Assess this cell for malaria.
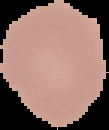
It is uninfected.

image_type: segmented cell region with the area outside set to black
image_size: 109×130 pixels
preparation: thin blood film